Locate every Plasmodium parasite.
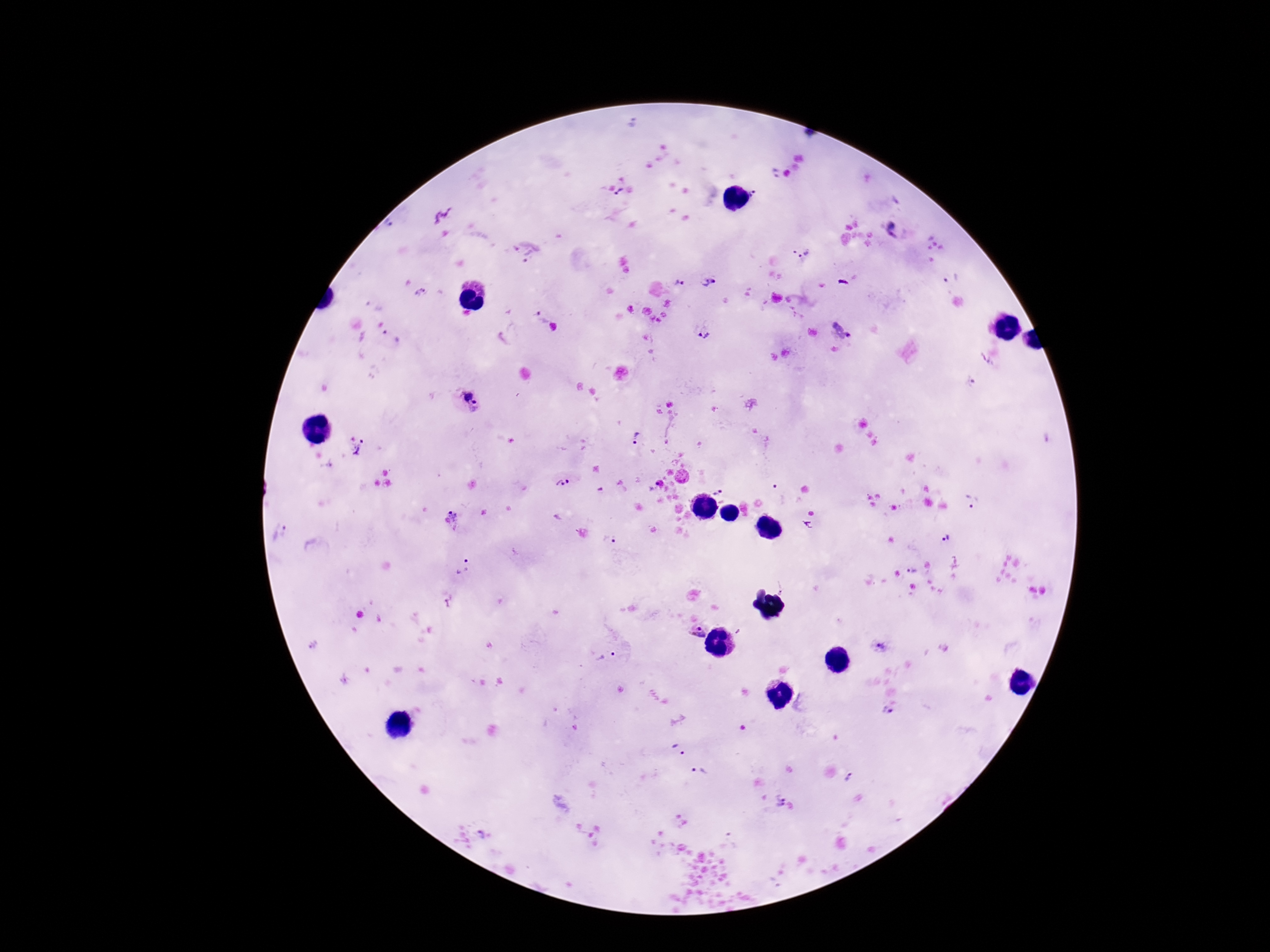
Approximate object centers, in pixels from the top-left corner.
Plasmodium parasites: (x=772, y=174), (x=620, y=192), (x=755, y=193), (x=892, y=230), (x=527, y=251), (x=799, y=252), (x=951, y=278), (x=707, y=282), (x=679, y=283), (x=421, y=292), (x=541, y=319), (x=703, y=334), (x=392, y=335), (x=972, y=381), (x=472, y=397), (x=636, y=439), (x=363, y=449), (x=563, y=483), (x=720, y=492), (x=972, y=502), (x=455, y=514), (x=806, y=525), (x=280, y=532), (x=945, y=536), (x=609, y=540), (x=462, y=568), (x=912, y=570), (x=697, y=633), (x=878, y=646), (x=608, y=656), (x=888, y=711), (x=678, y=749), (x=700, y=771), (x=849, y=778), (x=777, y=801), (x=482, y=835).

preparation = thick blood film
magnification = 100x
capture = smartphone camera through the microscope eyepiece
image size = 1270×952 pixels
patient malaria status = infected
stain = Giemsa
field of view = single